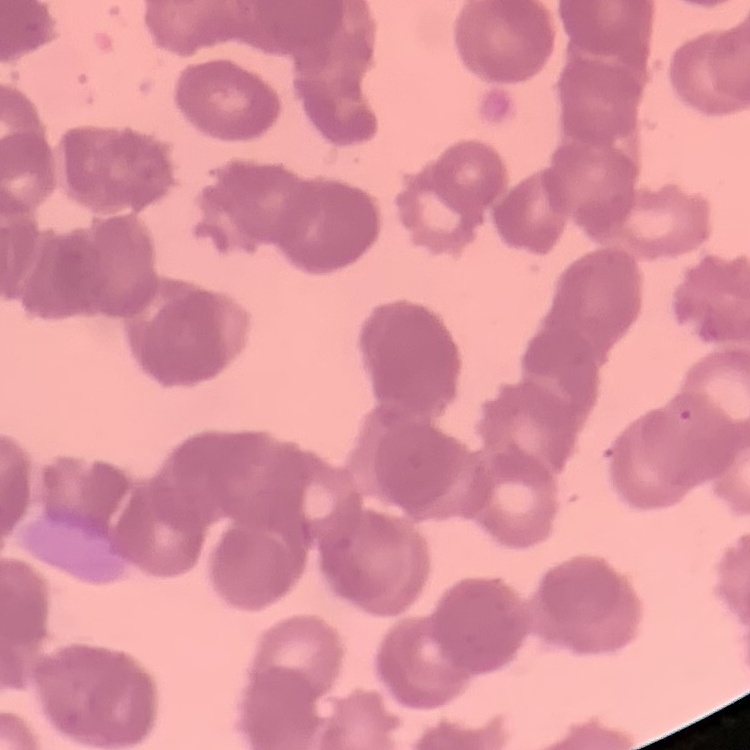

Summary:
  - Erythrocyte morphology: rouleaux formation
  - Preparation: thin blood smear
  - Stain: Field's or Giemsa
  - Image type: square crop of a larger photomicrograph